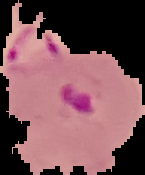

malaria status = parasitized
image size = 145×175 pixels
preparation = thin blood smear
image type = segmented cell region with the area outside set to black